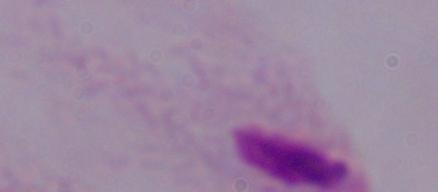
Summary:
  - Modality: photomicrograph
  - Identification: trichomonad
  - Magnification: 1000x